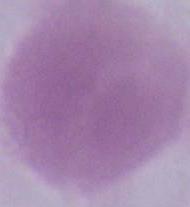

{
  "modality": "photomicrograph",
  "identification": "red blood cell",
  "magnification": "1000x"
}